Outline platelets.
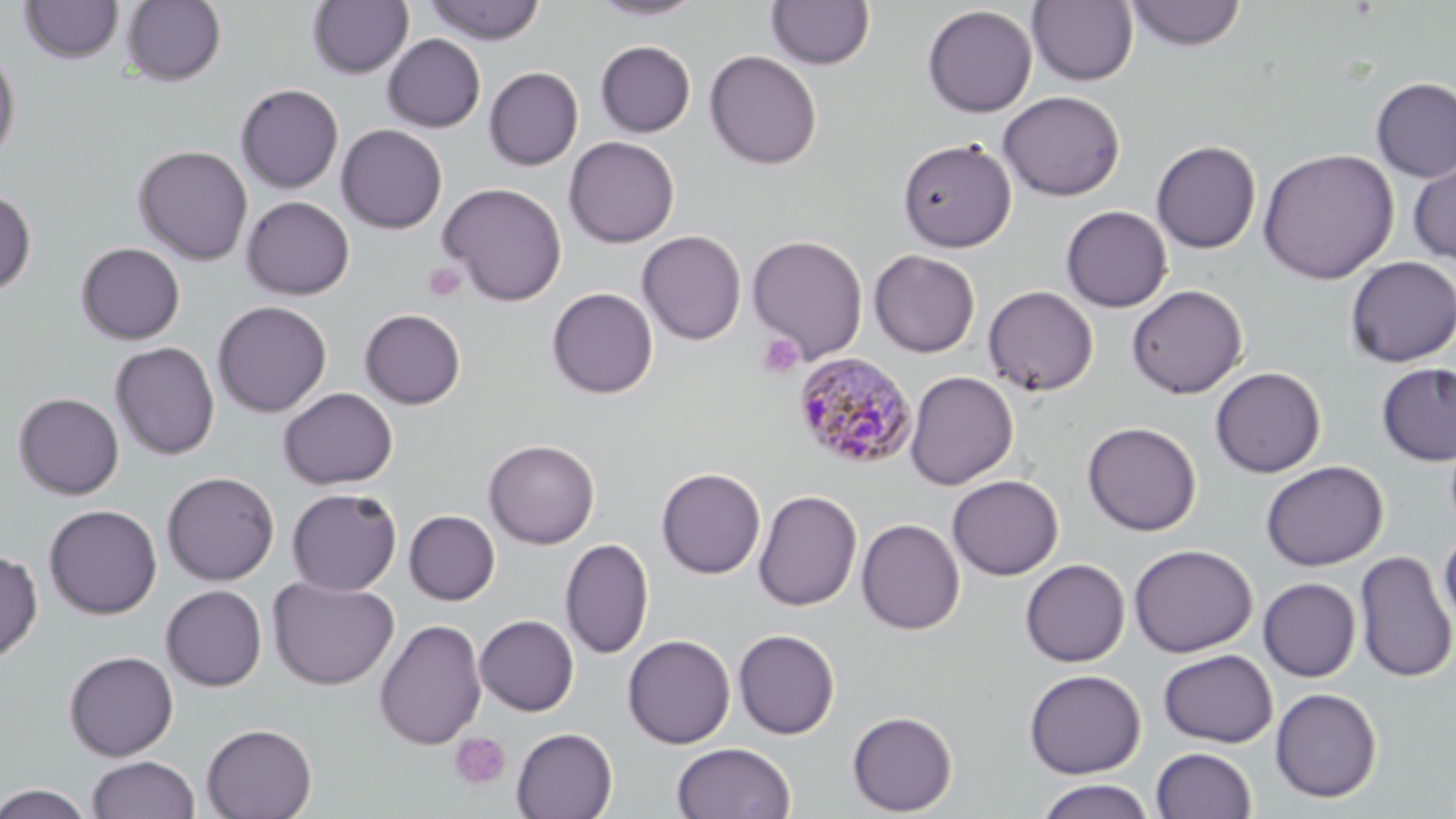
Approximate bounding boxes as (x1,y1)-(x2,y2) corner pairs in pixels.
Platelets: (423,263)-(466,302), (757,333)-(805,378), (450,731)-(511,790).

Summary:
  - Plasmodium malariae-infected red blood cell locations: (793,353)-(917,470)
  - Uninfected red blood cell locations: (425,0)-(546,45), (588,0)-(704,21), (19,1)-(125,64), (121,1)-(226,87), (307,1)-(414,79), (766,1)-(875,70), (1027,1)-(1139,86), (1125,1)-(1247,51), (922,5)-(1038,117), (382,34)-(486,133), (595,41)-(695,137), (0,46)-(22,165), (704,50)-(822,169), (484,67)-(583,170), (1371,77)-(1456,183), (235,83)-(344,194), (998,90)-(1125,201), (336,124)-(448,233), (564,136)-(680,248), (897,137)-(1017,253), (1151,140)-(1262,253), (132,145)-(254,266), (582,147)-(695,312), (1257,148)-(1399,285), (1407,154)-(1456,266), (438,182)-(568,306), (0,188)-(37,297), (241,196)-(355,300), (1060,205)-(1172,312), (637,230)-(746,345), (747,234)-(868,362), (76,242)-(185,344), (869,249)-(980,357), (1344,256)-(1456,367), (1126,284)-(1248,399), (983,285)-(1099,396), (547,287)-(658,399), (212,300)-(332,417), (359,308)-(466,409), (110,342)-(220,460), (1375,362)-(1456,466), (1210,367)-(1326,478), (905,371)-(1018,490), (279,387)-(398,489), (13,392)-(124,500), (1082,422)-(1201,536), (484,439)-(600,549), (1260,460)-(1389,571), (656,467)-(766,579), (162,471)-(280,585), (947,474)-(1063,580), (657,477)-(861,596), (286,488)-(402,596), (753,490)-(862,612), (44,504)-(162,619), (404,510)-(500,605), (856,518)-(964,635), (1439,530)-(1456,634), (559,537)-(655,660), (1128,543)-(1258,657), (0,548)-(42,664), (1354,550)-(1456,683), (1020,559)-(1130,667), (267,575)-(399,690), (1258,578)-(1361,682), (161,584)-(267,691), (475,614)-(579,716), (374,619)-(487,750), (733,629)-(840,739), (622,634)-(735,748), (1158,649)-(1277,747), (64,650)-(178,761), (1024,669)-(1146,778), (1269,687)-(1383,803), (847,710)-(958,816), (201,723)-(318,819), (511,727)-(618,819), (671,741)-(796,819), (1151,747)-(1257,819), (86,755)-(200,819), (1034,778)-(1157,818), (1,783)-(94,819)
  - Slide-level diagnosis: Plasmodium malariae
  - Preparation: thin blood film
  - Image size: 1456×819 pixels
  - Magnification: 1000x
  - Modality: light microscopy
  - Stain: May-Grünwald-Giemsa
  - Field of view: single